Assess the morphology of the red blood cells.
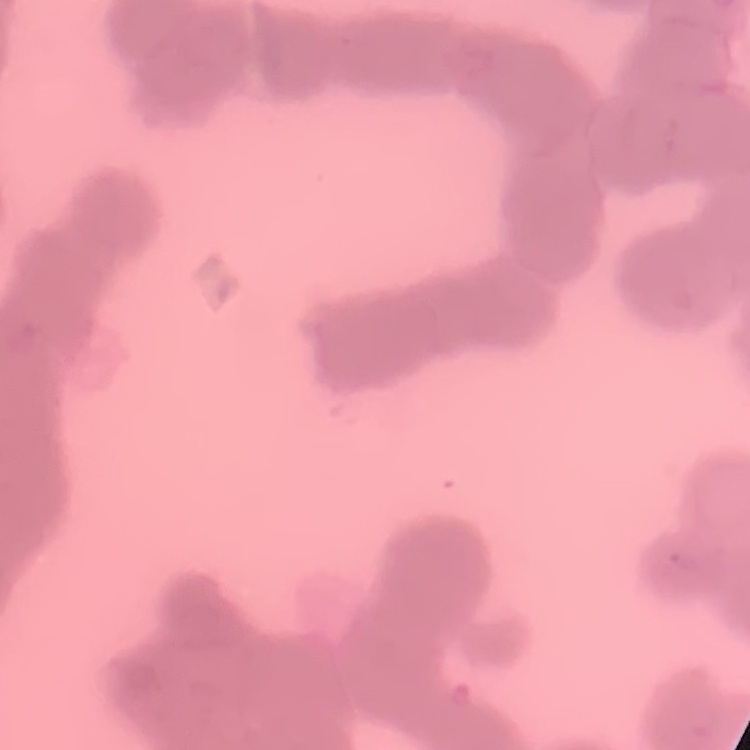

They show rouleaux formation.

stain = Field's or Giemsa
preparation = thin blood smear
image type = one tile cut from a larger photomicrograph